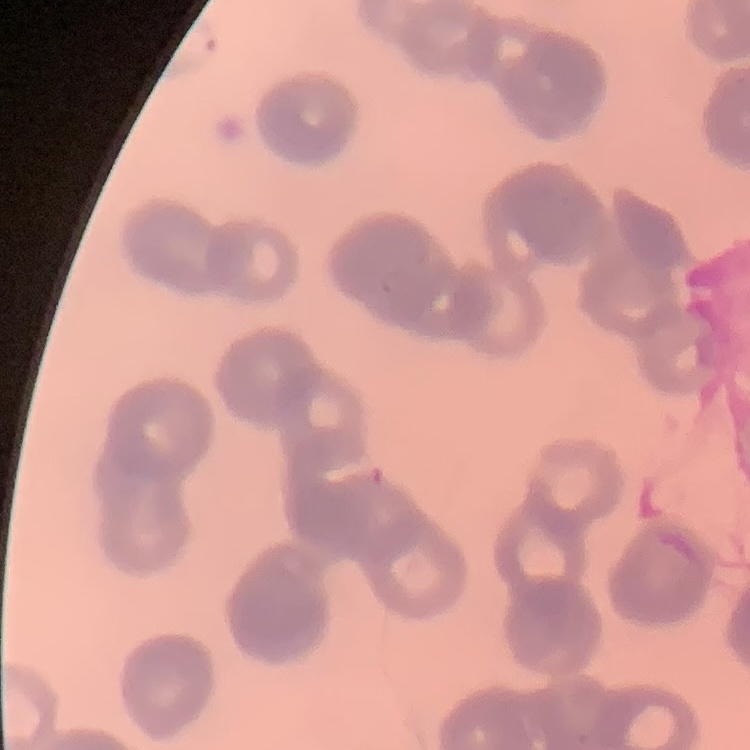

Summary:
  - Red blood cell morphology: rouleaux formation
  - Stain: Field's or Giemsa
  - Image type: one tile cut from a larger photomicrograph
  - Preparation: thin peripheral smear